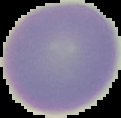
preparation = thin blood smear
image size = 121×118 pixels
result = no Plasmodium parasites seen
image type = cell region segmented out of the field of view; surrounding area masked to black